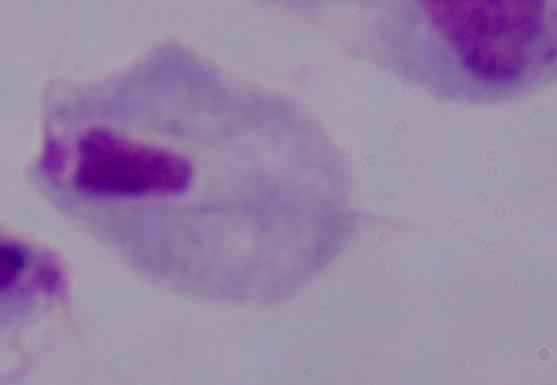 1000x magnification. Micrograph. A trichomonad is seen.